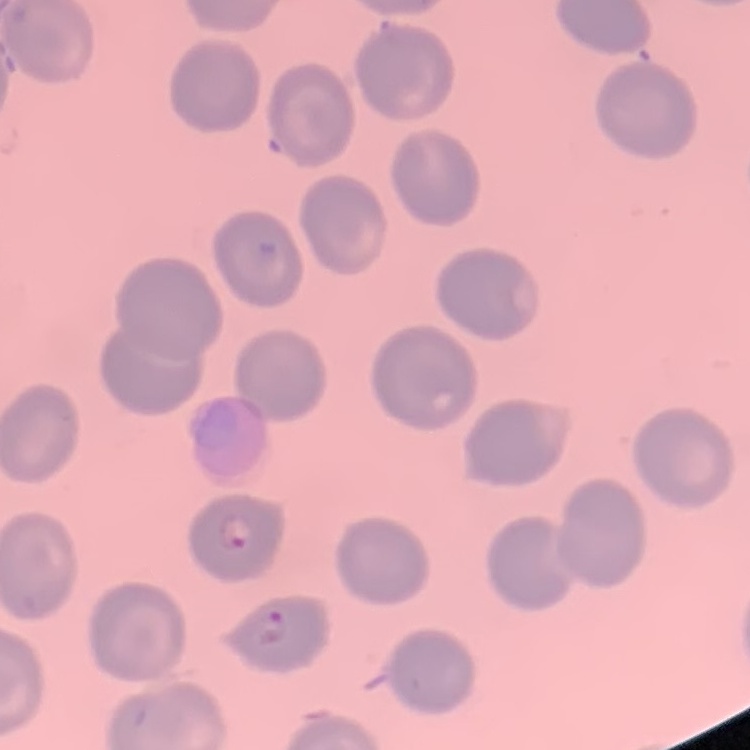
The red blood cells exhibit no rouleaux formation. Thin blood film. Stained with either Field's or Giemsa. Square crop of a larger photomicrograph.